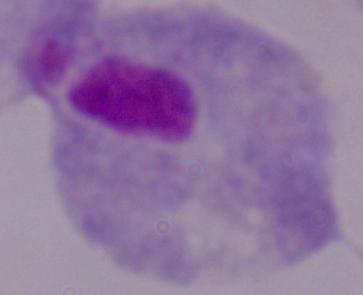 1000x magnification. A trichomonad is shown. Micrograph.